Give the position of every malaria parasite.
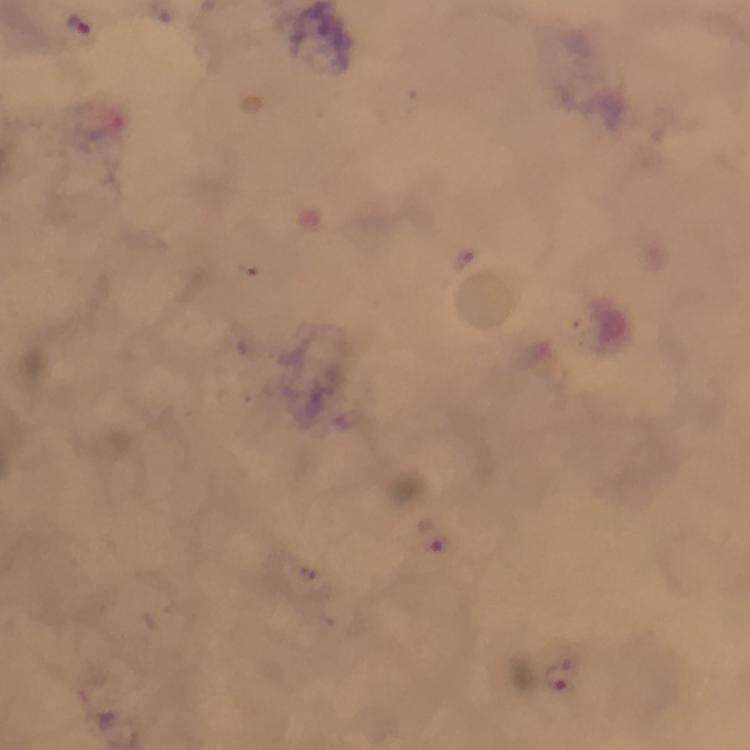

Approximate centers as {x, y} in pixels.
Malaria parasites: {80, 26}, {431, 536}, {556, 674}.

Summary:
  - Cropped from: one field of view
  - Magnification: 100x
  - Context: from a malaria diagnostic workup
  - Stain: Giemsa
  - Immersion oil: applied
  - Image size: 750×750 pixels
  - Preparation: thick blood smear
  - Capture: smartphone photograph through a microscope